Report the malaria status of this cell.
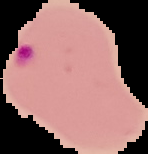
It is parasitized.

The area outside the segmented cell region is set to black. Image is 148×154 pixels. From a thin blood film.